Assess the morphology of the erythrocytes.
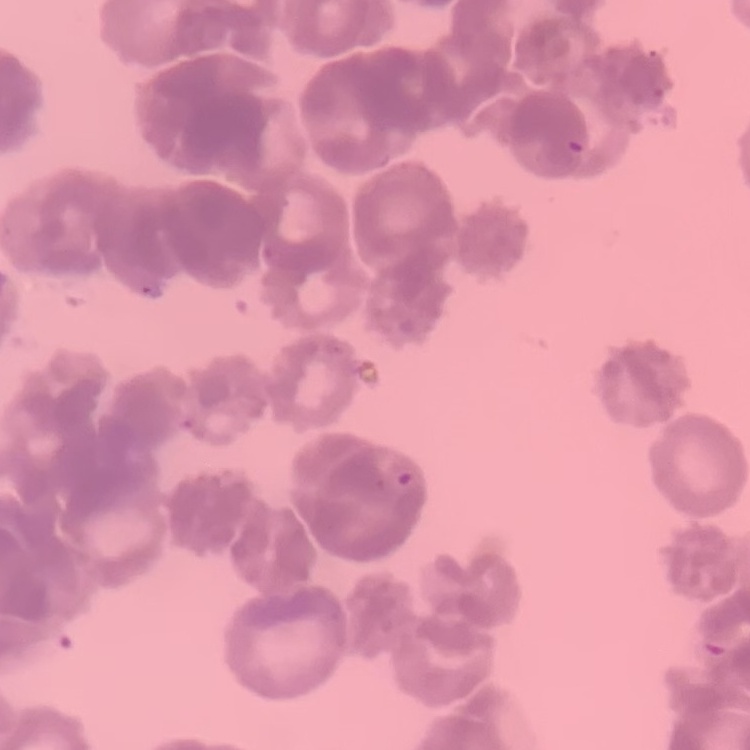
They show rouleaux formation.

Summary:
  - Stain: Field's or Giemsa
  - Image type: square crop of a larger photomicrograph
  - Preparation: thin peripheral smear